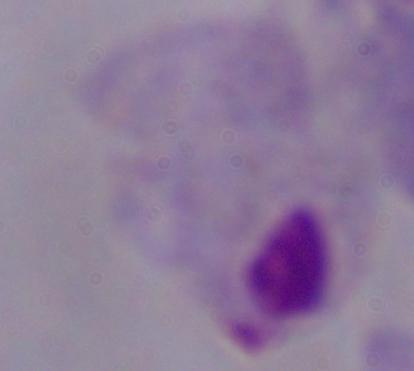
modality = photomicrograph
identification = trichomonad
magnification = 1000x